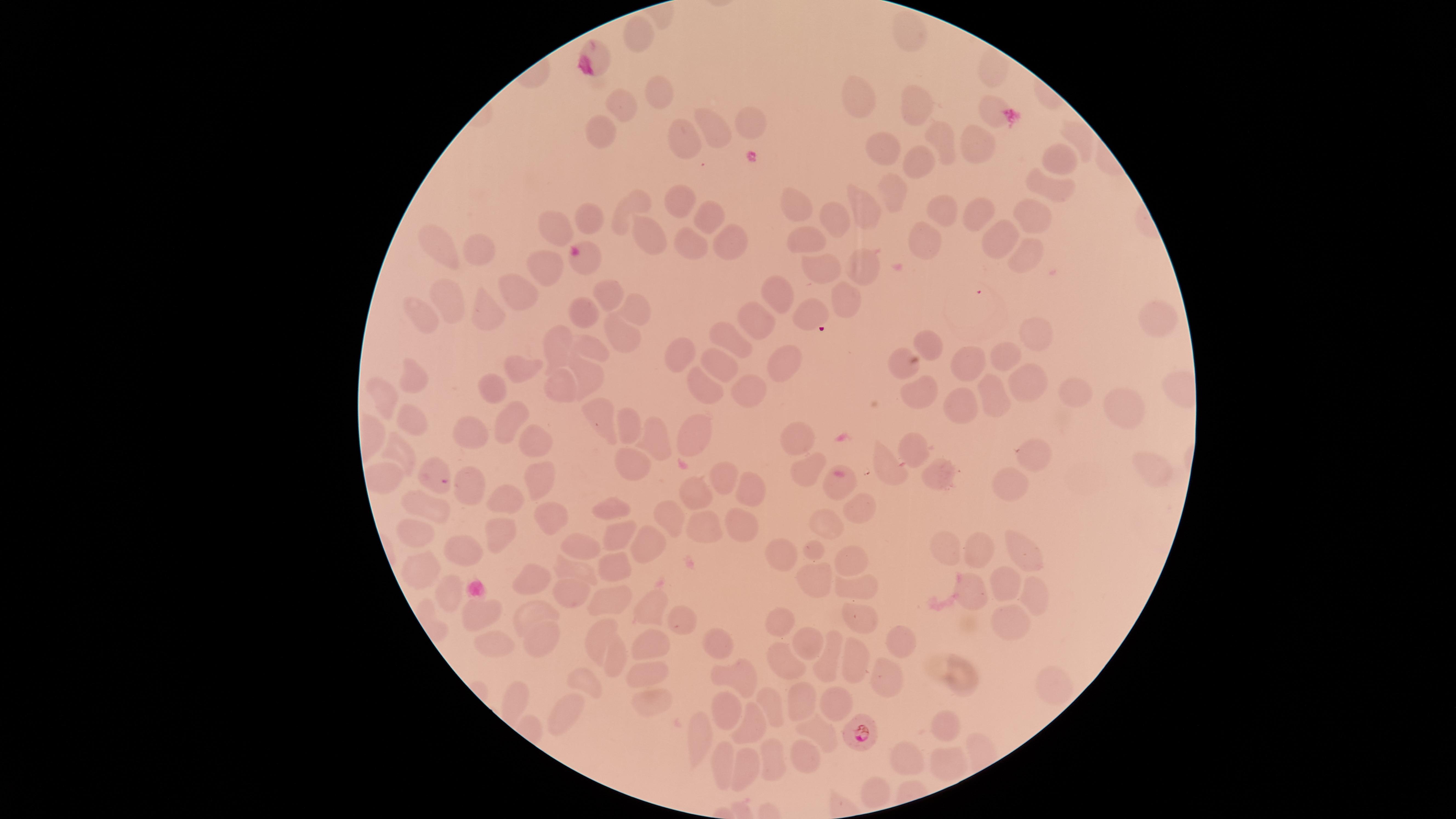
{
  "uninfected_RBCs": "approximate marker points as [x, y] in pixels: [906, 30], [634, 35], [593, 50], [993, 67], [653, 87], [857, 97], [621, 106], [916, 109], [990, 111], [751, 118], [599, 128], [710, 133], [1075, 139], [941, 140], [675, 145], [981, 147], [879, 148], [1057, 158], [919, 163], [1049, 182], [892, 195], [675, 202], [630, 206], [1035, 207], [942, 210], [799, 211], [705, 212], [862, 214], [973, 214], [837, 215], [587, 219], [554, 228], [645, 238], [730, 239], [996, 239], [691, 241], [808, 243], [448, 247], [926, 247], [477, 251], [1028, 254], [585, 260], [862, 261], [821, 265], [544, 272], [601, 292], [519, 293], [773, 294], [843, 296], [452, 298], [634, 305], [483, 309], [810, 313], [580, 316], [757, 316], [417, 318], [1155, 318], [1033, 333], [619, 335], [730, 341], [557, 343], [926, 343], [593, 351], [674, 355], [996, 355], [896, 359], [779, 360], [721, 361], [971, 363], [516, 372], [585, 372], [408, 376], [1031, 379], [700, 383], [754, 386], [560, 390], [1068, 390], [493, 391], [996, 395], [917, 396], [383, 405], [961, 406], [1129, 406], [506, 417], [599, 422], [630, 423], [414, 424], [693, 433], [472, 436], [533, 437], [797, 439], [655, 441], [912, 450], [399, 453], [1035, 453], [631, 460], [1149, 467], [885, 469], [803, 470], [936, 472], [385, 475], [724, 480], [533, 483], [469, 484], [835, 485], [1003, 485], [751, 489], [701, 491], [502, 499], [852, 505], [428, 507], [611, 508], [666, 512], [545, 520], [742, 522], [826, 522], [701, 524], [419, 530], [495, 533], [648, 535], [614, 538], [580, 544], [460, 546], [1023, 546], [947, 547], [983, 547], [813, 550], [785, 554], [847, 556], [613, 566], [579, 569], [421, 571], [819, 577], [1002, 581], [533, 586], [857, 588], [968, 591], [1033, 593], [447, 594], [572, 596], [604, 601], [538, 606], [642, 607], [856, 614], [483, 616], [782, 619], [1010, 620], [679, 621], [596, 632], [540, 640], [901, 640], [715, 641], [649, 645], [808, 645], [499, 648], [854, 655], [781, 657], [618, 660], [830, 660], [650, 671], [887, 671], [956, 671], [742, 679], [586, 684], [1050, 688], [515, 697], [803, 701], [835, 702], [648, 704], [565, 708], [722, 708], [773, 711], [947, 721], [750, 726], [827, 732], [696, 735], [914, 757], [948, 757], [803, 760], [715, 761], [772, 762], [743, 768], [876, 788]",
  "capture": "smartphone photograph through the microscope eyepiece",
  "field_of_view": "single",
  "image_size": "1456×819 pixels",
  "species": "Plasmodium falciparum",
  "stain": "Giemsa",
  "visible_region": "circular",
  "preparation": "thin smear of blood",
  "presence": "malaria parasites seen",
  "parasitized_RBCs": "approximate marker points as [x, y] in pixels: [438, 479], [856, 732]"
}